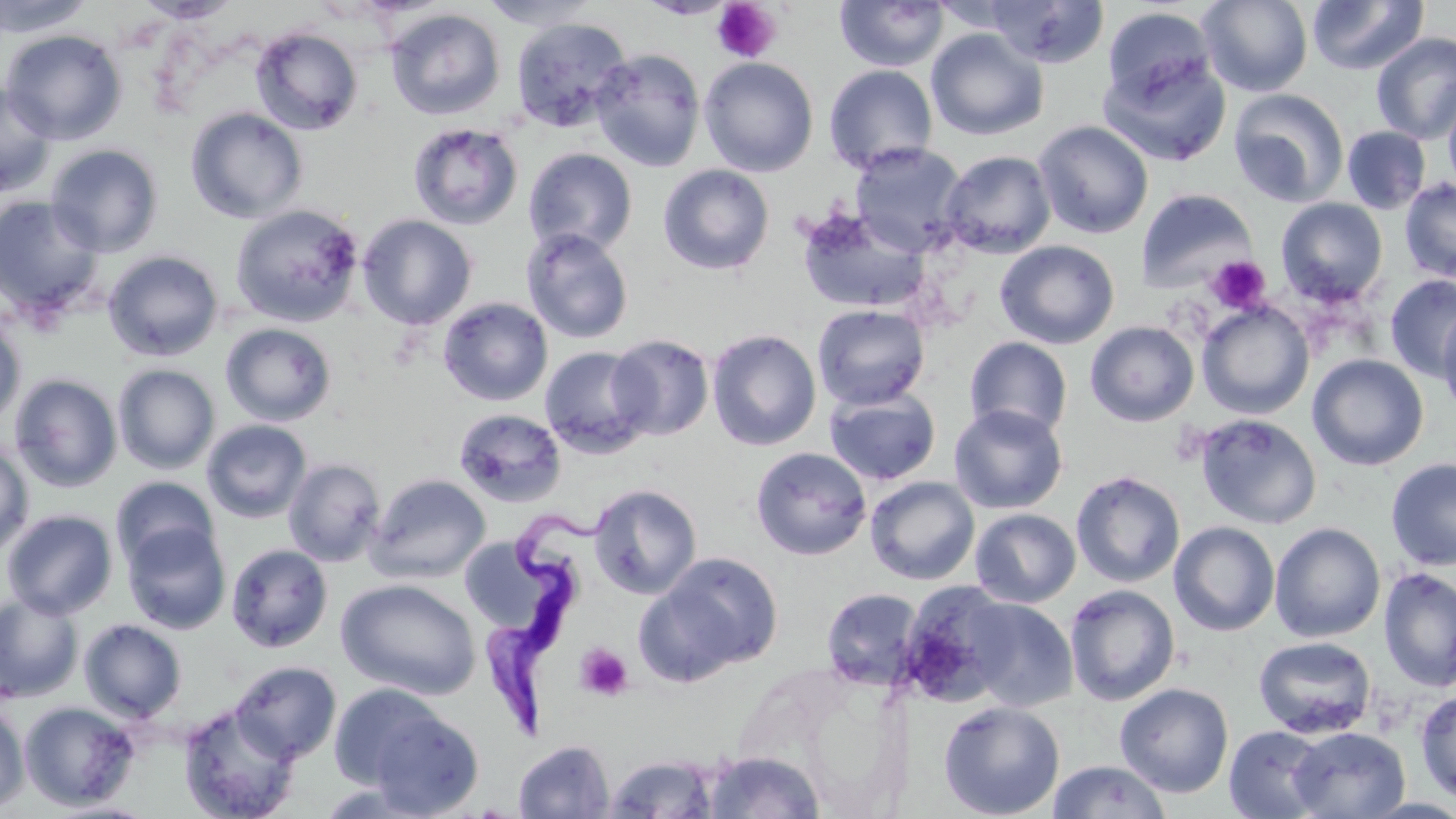

slide-level diagnosis = Trypanosoma brucei
image size = 1456×819 pixels
preparation = thin blood film
stain = May-Grünwald-Giemsa
platelet locations = approximate bounding boxes as [x1, y1, x2, y2] in pixels: [711, 1, 782, 64], [1205, 255, 1271, 314], [574, 643, 634, 701]
Trypanosoma brucei locations = approximate bounding boxes as [x1, y1, x2, y2] in pixels: [477, 505, 613, 741]
field of view = one of a larger specimen
modality = light microscopy
magnification = 1000x
uninfected red blood cell locations = approximate bounding boxes as [x1, y1, x2, y2] in pixels: [0, 0, 96, 38], [133, 0, 243, 24], [479, 0, 603, 30], [983, 0, 1110, 69], [1198, 0, 1313, 96], [1307, 0, 1429, 75], [835, 1, 950, 72], [1101, 5, 1217, 107], [385, 7, 505, 121], [510, 17, 633, 133], [251, 26, 364, 136], [925, 27, 1048, 141], [1, 29, 127, 145], [1371, 32, 1456, 144], [589, 48, 706, 172], [1098, 52, 1231, 168], [698, 56, 819, 177], [823, 64, 938, 174], [0, 81, 57, 198], [1442, 83, 1456, 196], [1229, 89, 1349, 207], [185, 107, 308, 224], [1033, 120, 1154, 239], [408, 122, 524, 231], [1341, 126, 1432, 214], [848, 142, 968, 256], [46, 144, 164, 257], [523, 147, 638, 257], [939, 150, 1057, 258], [658, 164, 775, 276], [1398, 178, 1456, 283], [1138, 188, 1257, 293], [0, 195, 104, 319], [1276, 197, 1389, 305], [229, 203, 365, 327], [795, 206, 932, 315], [357, 214, 478, 330], [520, 228, 634, 344], [994, 240, 1120, 349], [102, 250, 224, 361], [1384, 274, 1456, 381], [438, 297, 553, 406], [1196, 301, 1314, 419], [812, 304, 931, 410], [1437, 306, 1456, 418], [0, 311, 27, 431], [1085, 321, 1200, 426], [220, 323, 338, 426], [707, 329, 821, 451], [607, 334, 714, 440], [964, 336, 1073, 440], [538, 346, 654, 459], [1307, 353, 1429, 471], [112, 364, 220, 474], [9, 373, 122, 492], [824, 388, 942, 486], [948, 404, 1068, 514], [453, 408, 567, 507], [1193, 412, 1322, 529], [201, 419, 312, 523], [0, 438, 35, 558], [750, 446, 872, 561], [283, 458, 386, 567], [1385, 458, 1456, 570], [1070, 470, 1186, 588], [367, 474, 491, 583], [111, 476, 221, 571], [865, 476, 980, 585], [588, 484, 702, 599], [970, 508, 1081, 608], [2, 509, 118, 619], [1168, 521, 1280, 637], [122, 522, 231, 634], [1269, 522, 1386, 643], [225, 543, 333, 653], [465, 543, 566, 635], [638, 551, 785, 684], [1378, 566, 1456, 693], [337, 578, 481, 700], [897, 583, 1017, 708], [1063, 584, 1180, 706], [821, 587, 923, 691], [0, 592, 84, 703], [960, 597, 1079, 711], [78, 618, 187, 722], [1253, 635, 1377, 739], [231, 660, 342, 762], [1114, 682, 1234, 797], [1415, 689, 1456, 804], [345, 692, 484, 816], [938, 700, 1065, 819], [19, 701, 140, 811], [178, 702, 302, 819], [0, 704, 29, 813], [1223, 724, 1330, 819], [1288, 726, 1410, 818], [513, 740, 615, 819], [703, 751, 825, 817], [603, 754, 721, 818], [1046, 760, 1172, 818], [43, 800, 162, 818]